Outline platelets.
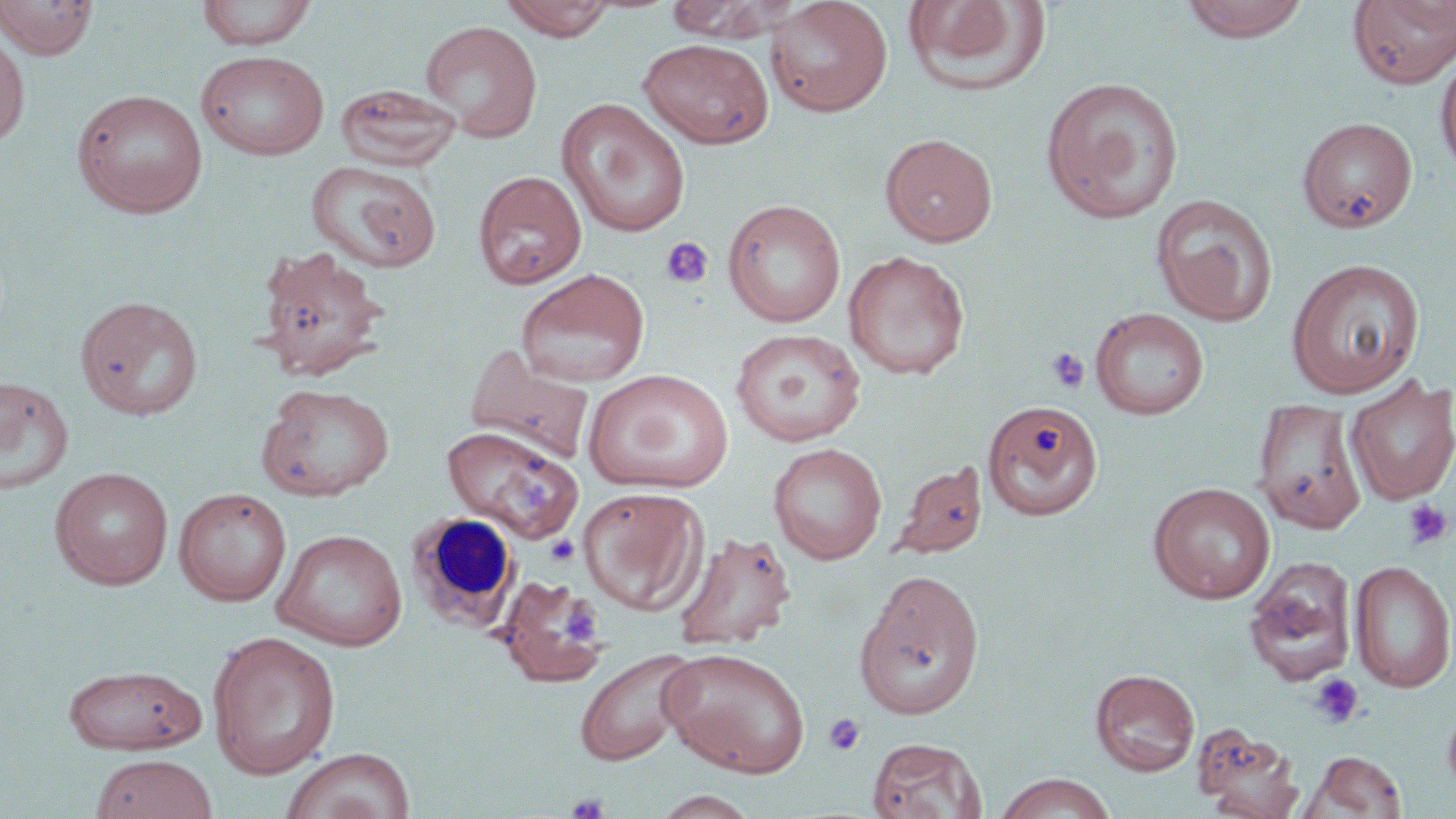

Approximate bounding boxes as (x1,y1)-(x2,y2) corner pairs in pixels.
Platelets: (660,237)-(714,290), (1046,347)-(1090,394), (1402,499)-(1453,550), (546,534)-(580,566), (557,603)-(603,644), (1308,672)-(1365,730), (823,713)-(866,756), (566,791)-(611,818).

{
  "slide_level_diagnosis": "negative for blood parasites",
  "modality": "light microscopy",
  "magnification": "1000x",
  "white_blood_cell_locations": "approximate bounding boxes as (x1,y1)-(x2,y2) corner pairs in pixels: (406,512)-(521,631)",
  "uninfected_red_blood_cell_locations": "approximate bounding boxes as (x1,y1)-(x2,y2) corner pairs in pixels: (0,0)-(98,59), (196,0)-(318,50), (500,0)-(618,41), (664,0)-(796,43), (764,0)-(893,117), (903,0)-(1052,97), (1178,0)-(1313,44), (1349,1)-(1456,89), (419,20)-(544,142), (0,29)-(30,148), (638,38)-(775,149), (195,49)-(330,160), (1435,49)-(1456,180), (1040,76)-(1185,224), (335,83)-(462,172), (72,88)-(209,218), (556,98)-(691,238), (1297,116)-(1418,234), (880,133)-(998,247), (306,160)-(441,273), (473,170)-(587,290), (1150,193)-(1279,327), (722,199)-(847,327), (253,245)-(389,382), (843,251)-(970,380), (1285,257)-(1426,398), (515,268)-(650,388), (75,295)-(203,420), (1090,307)-(1210,419), (730,328)-(866,447), (464,344)-(595,464), (584,369)-(733,493), (1345,375)-(1456,506), (0,378)-(74,493), (258,383)-(394,501), (982,400)-(1103,521), (1254,400)-(1366,533), (441,426)-(583,543), (767,442)-(888,564), (890,459)-(988,558), (50,467)-(174,590), (1149,482)-(1275,604), (578,486)-(707,615), (174,487)-(291,605), (272,528)-(408,650), (674,530)-(797,652), (1350,559)-(1456,692), (1243,561)-(1356,687), (854,571)-(986,720), (496,575)-(610,687), (207,630)-(341,779), (659,646)-(811,778), (573,647)-(698,765), (62,664)-(208,755), (1090,668)-(1200,776), (1442,696)-(1456,797), (1194,724)-(1303,818), (866,737)-(987,818), (280,747)-(415,819), (1303,750)-(1408,818), (89,754)-(219,819), (994,772)-(1117,819), (651,790)-(761,818)",
  "field_of_view": "single",
  "preparation": "thin blood smear",
  "stain": "May-Grünwald-Giemsa",
  "image_size": "1456×819 pixels"
}